Assess this cell for malaria.
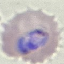

Parasitized.

Giemsa-stained preparation. Acquired by smartphone through the microscope eyepiece. Thin blood film. Automatically extracted cell patch, resized to 64 × 64 pixels.